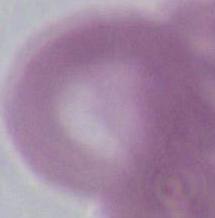
Summary:
  - Modality: photomicrograph
  - Magnification: 1000x
  - Identification: red blood cell